Report the malaria status of this cell.
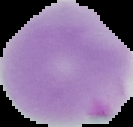
It is parasitized.

image type = segmented cell region with the area outside set to black
image size = 133×127 pixels
preparation = thin blood smear